State which parasite is depicted.
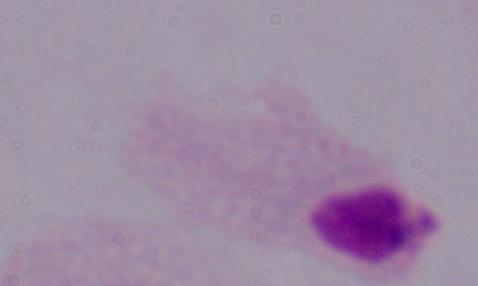

This is a trichomonad.

Photomicrograph. Captured at 1000x magnification.